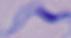

Summary:
  - Identification: trypanosome
  - Modality: photomicrograph
  - Magnification: 1000x